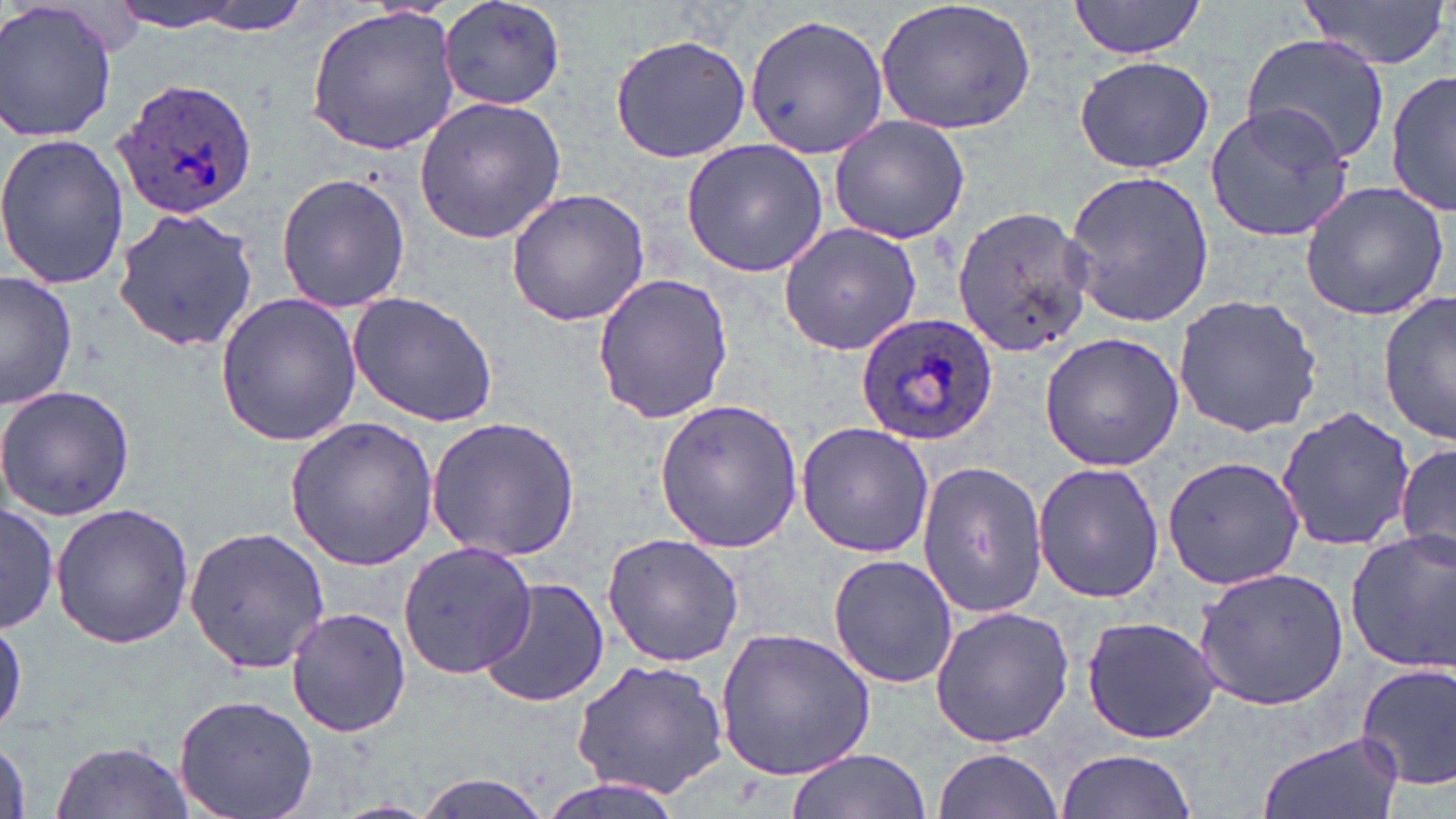
Approximate bounding boxes as [x1, y1, x2, y2] in pixels. Plasmodium ovale-infected red blood cell locations: [114, 75, 261, 221], [855, 311, 998, 445]. Uninfected red blood cell locations: [0, 0, 119, 143], [156, 0, 318, 35], [441, 0, 566, 111], [874, 0, 1038, 136], [1301, 0, 1449, 73], [1068, 1, 1207, 58], [105, 3, 252, 32], [304, 7, 462, 154], [742, 13, 891, 161], [1242, 32, 1394, 169], [609, 33, 751, 164], [1073, 55, 1213, 173], [1387, 71, 1454, 217], [414, 95, 566, 243], [1203, 103, 1356, 243], [827, 115, 973, 245], [0, 133, 128, 290], [681, 138, 827, 278], [1061, 168, 1214, 327], [275, 171, 410, 314], [1299, 179, 1450, 322], [504, 187, 651, 328], [950, 203, 1097, 358], [111, 207, 262, 353], [777, 219, 922, 356], [591, 272, 733, 424], [1, 273, 79, 410], [1379, 290, 1455, 445], [346, 291, 501, 428], [213, 292, 364, 446], [1172, 294, 1323, 437], [1037, 332, 1185, 472], [0, 386, 134, 519], [653, 397, 805, 554], [1277, 407, 1416, 554], [283, 417, 439, 570], [425, 417, 582, 561], [795, 422, 934, 558], [1396, 445, 1456, 566], [1160, 455, 1302, 590], [915, 460, 1048, 620], [1032, 461, 1166, 602], [49, 501, 194, 650], [1, 502, 58, 634], [184, 524, 332, 676], [1345, 532, 1455, 673], [601, 534, 745, 667], [398, 540, 534, 680], [826, 553, 959, 689], [1193, 566, 1349, 711], [476, 576, 610, 710], [285, 606, 411, 738], [929, 606, 1074, 747], [1079, 613, 1224, 745], [715, 627, 877, 783], [568, 655, 730, 800], [1355, 661, 1456, 791], [173, 693, 317, 819], [1256, 730, 1405, 819], [49, 740, 196, 818], [934, 746, 1064, 816], [784, 748, 929, 819], [1053, 749, 1201, 819], [412, 772, 558, 819], [534, 778, 682, 819]. Slide-level diagnosis: Plasmodium ovale. One field of a larger specimen. Thin blood smear. Image is 1456×819 pixels. May-Grünwald-Giemsa stain. Light microscopy. Captured at 1000x magnification.